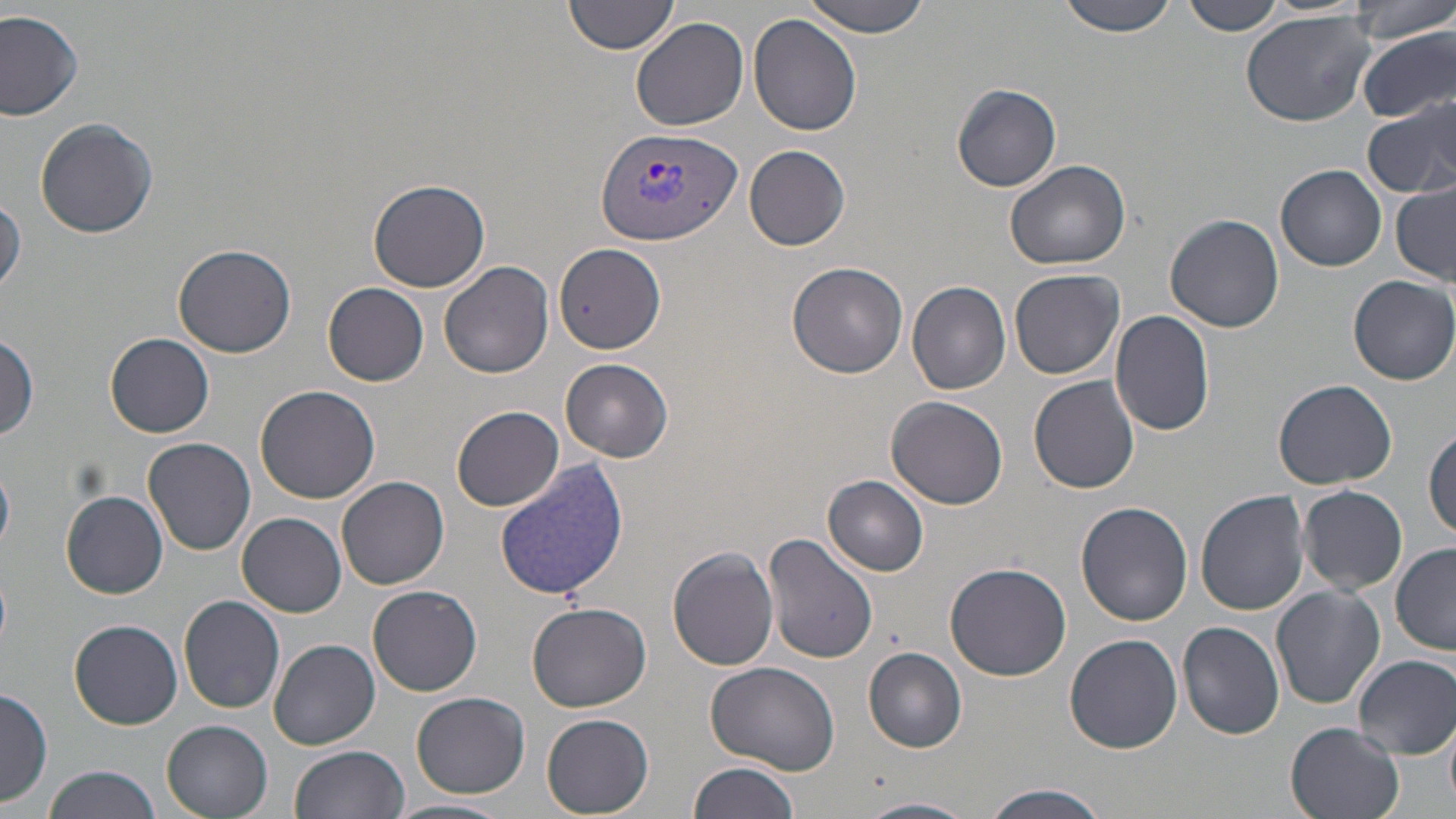

slide-level diagnosis = Plasmodium vivax
magnification = 1000x
preparation = thin blood smear
Plasmodium vivax-infected red blood cell locations = approximate bounding boxes as [x1, y1, x2, y2] in pixels: [595, 125, 745, 244]
image size = 1456×819 pixels
stain = May-Grünwald-Giemsa
field of view = single
modality = light microscopy
uninfected red blood cell locations = approximate bounding boxes as [x1, y1, x2, y2] in pixels: [565, 0, 681, 56], [796, 0, 938, 36], [1058, 0, 1177, 38], [1349, 0, 1454, 44], [1180, 1, 1285, 36], [0, 9, 84, 120], [1240, 9, 1377, 128], [748, 14, 863, 136], [631, 16, 748, 131], [1358, 27, 1456, 123], [952, 84, 1060, 192], [1363, 97, 1456, 200], [35, 118, 161, 240], [746, 145, 850, 250], [1004, 159, 1133, 271], [1278, 165, 1387, 272], [369, 178, 490, 292], [1392, 184, 1456, 283], [0, 197, 25, 297], [1165, 214, 1285, 332], [556, 244, 668, 353], [173, 245, 296, 358], [441, 261, 553, 380], [787, 262, 909, 379], [1008, 268, 1125, 379], [1348, 275, 1456, 385], [907, 281, 1011, 394], [323, 282, 429, 384], [1109, 310, 1216, 437], [104, 332, 215, 439], [0, 335, 40, 441], [560, 357, 673, 460], [1029, 375, 1139, 494], [1275, 378, 1396, 489], [254, 382, 381, 503], [886, 396, 1009, 510], [453, 404, 564, 511], [1424, 428, 1456, 540], [144, 436, 256, 555], [495, 461, 628, 601], [337, 475, 451, 589], [823, 475, 930, 577], [1297, 484, 1408, 595], [1194, 489, 1309, 615], [61, 491, 168, 598], [1075, 502, 1193, 626], [237, 513, 347, 616], [761, 533, 878, 665], [1390, 544, 1455, 656], [667, 546, 779, 671], [944, 561, 1072, 681], [369, 585, 482, 694], [1270, 586, 1385, 710], [179, 596, 286, 715], [526, 601, 652, 712], [69, 619, 183, 729], [1178, 621, 1285, 739], [1064, 634, 1183, 754], [269, 638, 379, 749], [863, 647, 968, 751], [1353, 654, 1456, 760], [704, 660, 842, 776], [0, 688, 52, 808], [411, 691, 530, 799], [540, 713, 655, 818], [1445, 717, 1456, 811], [161, 719, 273, 817], [1285, 722, 1407, 819], [291, 745, 411, 819], [687, 761, 798, 819], [41, 766, 162, 819], [983, 784, 1112, 819], [391, 797, 512, 819], [858, 797, 975, 819]